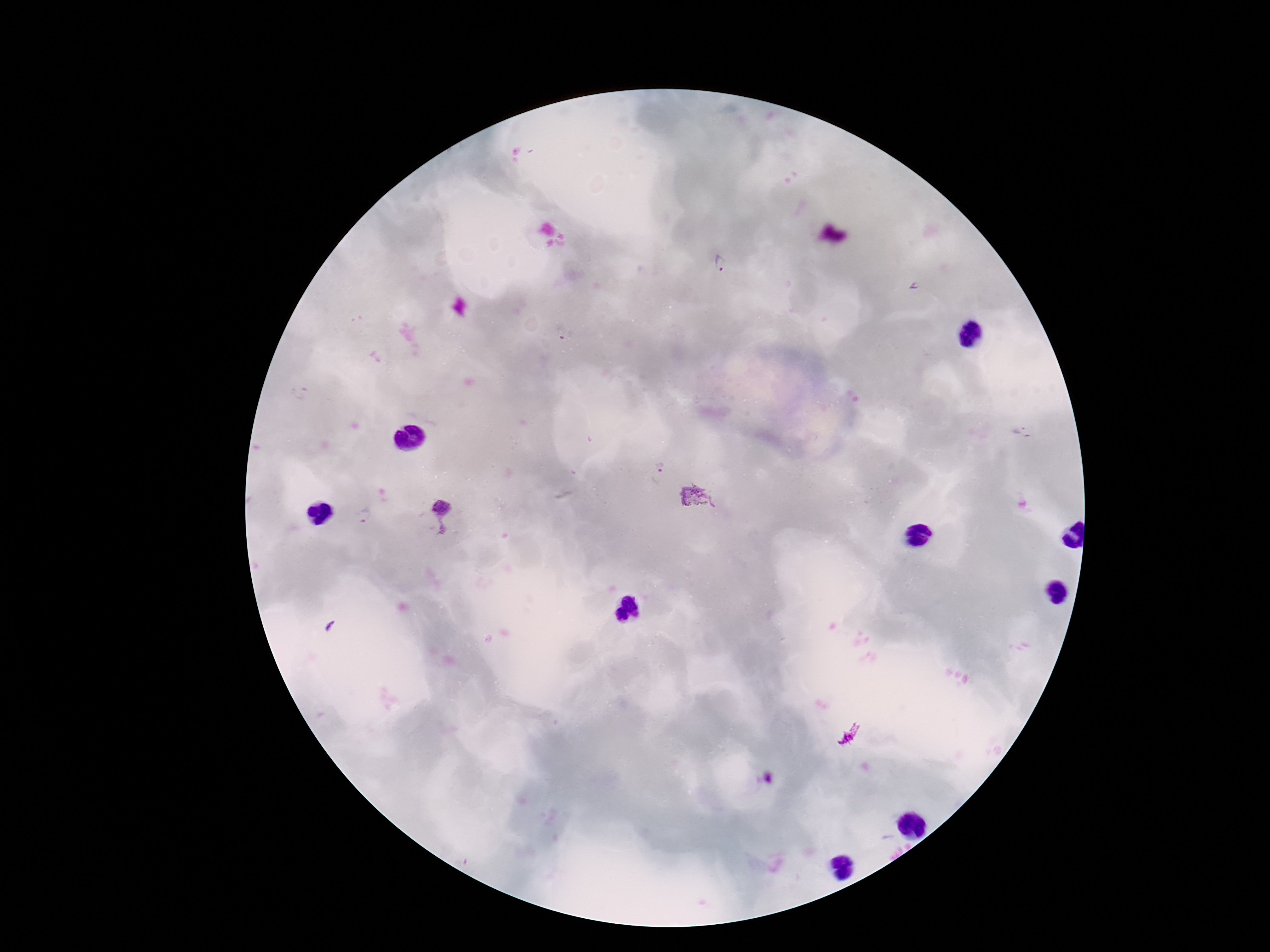
patient malaria status = infected
stain = Giemsa
image size = 1270×952 pixels
capture = smartphone camera through the microscope eyepiece
Plasmodium parasite locations = approximate object centers, in pixels from the top-left corner: (x=720, y=263), (x=914, y=286), (x=656, y=472), (x=699, y=498), (x=367, y=516), (x=443, y=518), (x=330, y=625)
preparation = thick peripheral-blood smear
magnification = 100x
field of view = one from this slide